Assess the morphology of the erythrocytes.
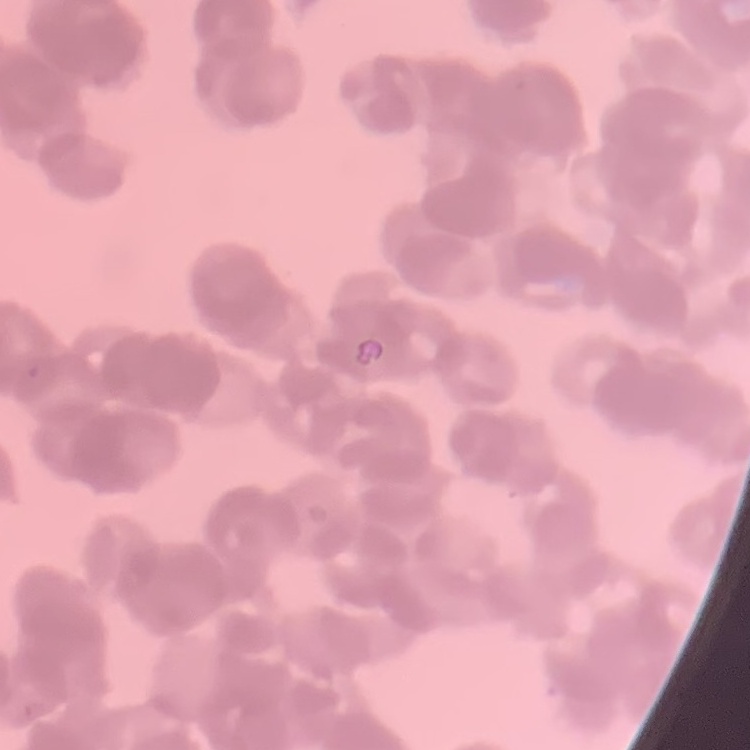
Rouleaux formation.

{
  "stain": "Field's or Giemsa",
  "preparation": "thin blood smear",
  "image_type": "square crop of a larger photomicrograph"
}